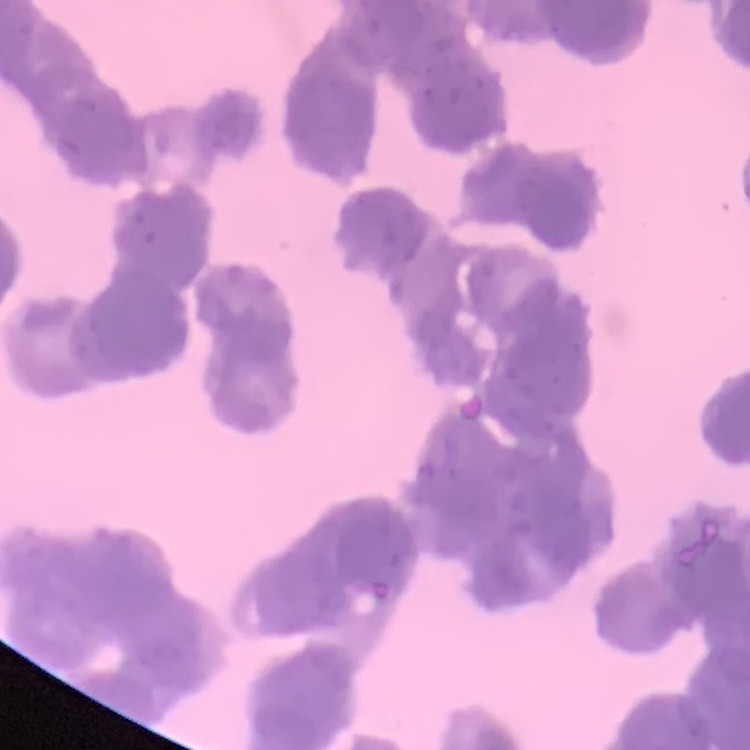
The red blood cells exhibit rouleaux formation. Thin blood film. One tile cut from a larger photomicrograph. Field's or Giemsa stain.